Assess this cell for malaria.
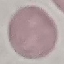

It is uninfected.

image type = cell patch, automatically extracted from a larger field of view and resized to 64 × 64 pixels
capture = smartphone through the microscope eyepiece
stain = Giemsa
preparation = thin blood film